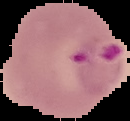 The area outside the segmented cell region is set to black. Image is 130×121 pixels. From a thin blood film. Result: malaria parasites identified.